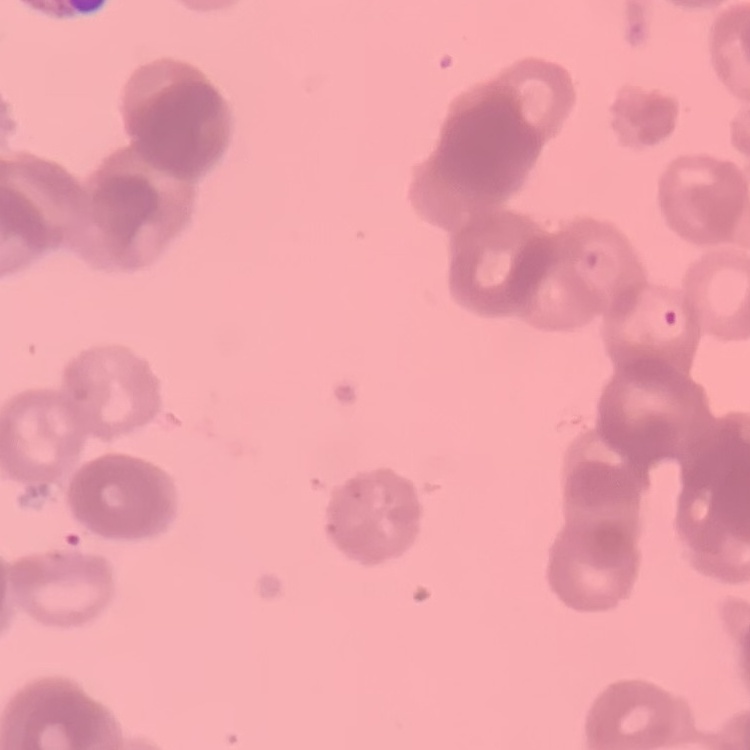

The erythrocytes exhibit rouleaux formation. One tile cut from a larger photomicrograph. Thin blood smear. Field's or Giemsa stain.